Identify the parasite.
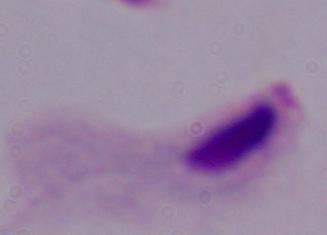
A trichomonad.

magnification = 1000x
modality = micrograph